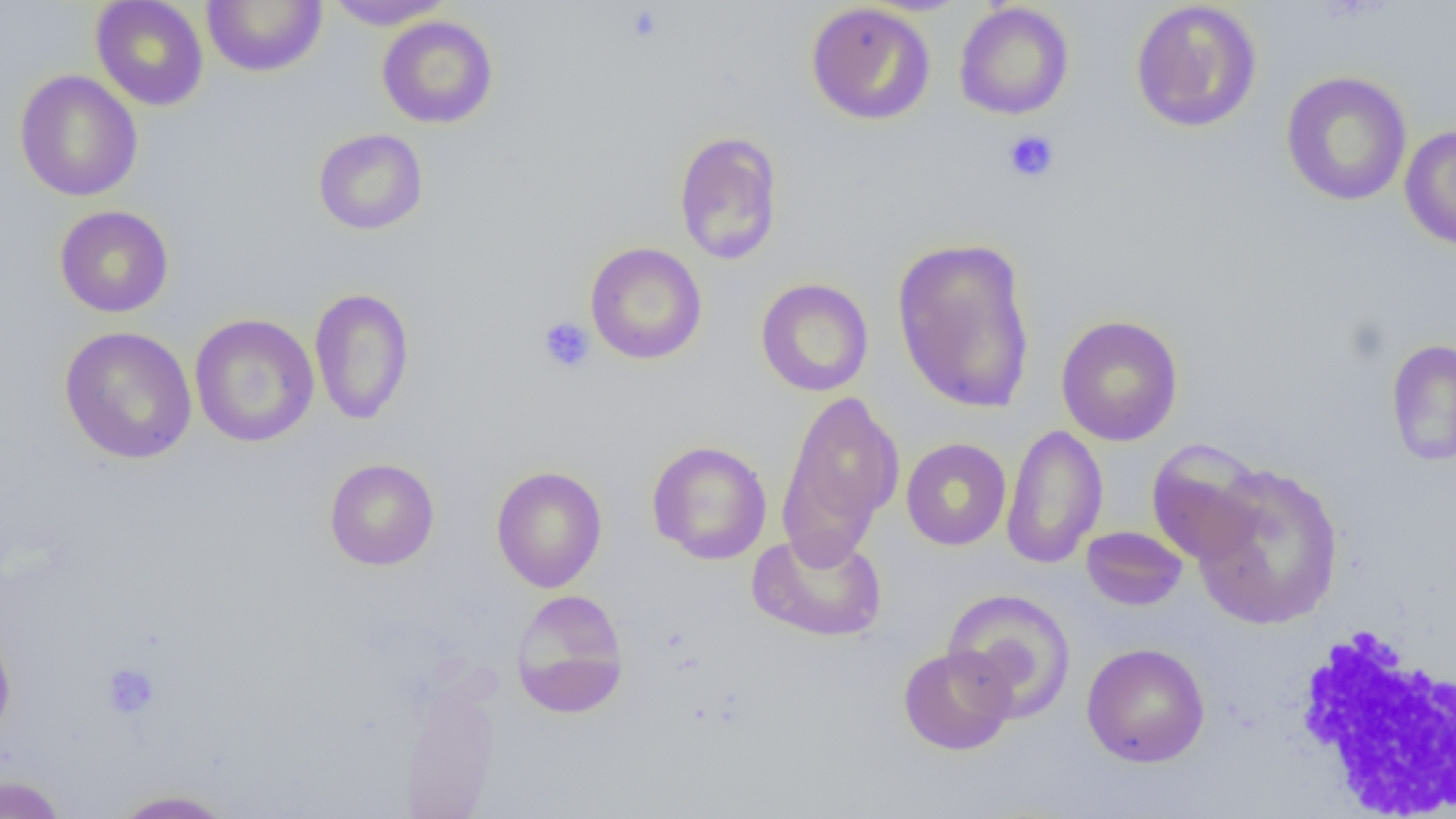
{
  "slide_level_diagnosis": "no evidence of blood parasites",
  "white_blood_cell_locations": "approximate bounding boxes as (x1, y1, x2, y2) in pixels: (1288, 622, 1456, 817)",
  "modality": "optical microscopy",
  "uninfected_red_blood_cell_locations": "approximate bounding boxes as (x1, y1, x2, y2) in pixels: (90, 0, 209, 111), (201, 0, 327, 77), (323, 0, 455, 30), (1130, 1, 1263, 133), (805, 2, 936, 126), (954, 3, 1075, 120), (377, 15, 499, 129), (14, 69, 143, 202), (1280, 70, 1413, 207), (1399, 124, 1456, 250), (313, 128, 429, 235), (673, 130, 784, 266), (53, 205, 174, 318), (891, 236, 1037, 414), (585, 242, 707, 364), (755, 278, 874, 397), (309, 287, 415, 426), (189, 313, 320, 448), (1055, 314, 1184, 446), (59, 325, 197, 465), (1386, 338, 1456, 467), (776, 388, 904, 560), (1000, 423, 1108, 570), (900, 437, 1012, 551), (646, 440, 772, 564), (1146, 440, 1270, 567), (324, 457, 439, 571), (1191, 461, 1344, 630), (491, 465, 608, 593), (1081, 525, 1188, 611), (746, 527, 888, 643), (511, 588, 629, 717), (942, 588, 1076, 721), (0, 619, 17, 744), (1082, 642, 1210, 767), (897, 645, 1016, 756), (399, 676, 502, 817), (0, 775, 68, 818), (108, 789, 237, 818)",
  "preparation": "thin blood smear",
  "image_size": "1456×819 pixels",
  "field_of_view": "single",
  "magnification": "1000x",
  "platelet_locations": "approximate bounding boxes as (x1, y1, x2, y2) in pixels: (624, 5, 665, 45), (1003, 129, 1060, 183), (537, 316, 596, 373), (101, 663, 160, 719)"
}